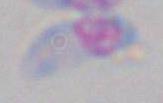

Toxoplasma gondii is shown. Photomicrograph. Captured at 1000x magnification.